Assess this cell for malaria.
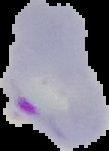

It is parasitized.

Summary:
  - Preparation: thin blood smear
  - Image size: 109×151 pixels
  - Image type: segmented cell region on a black background